Report the malaria status of this cell.
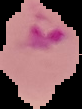
It is parasitized.

Image is 82×109 pixels. From a thin blood smear. Cell region segmented out of the field of view; the surrounding area is masked to black.